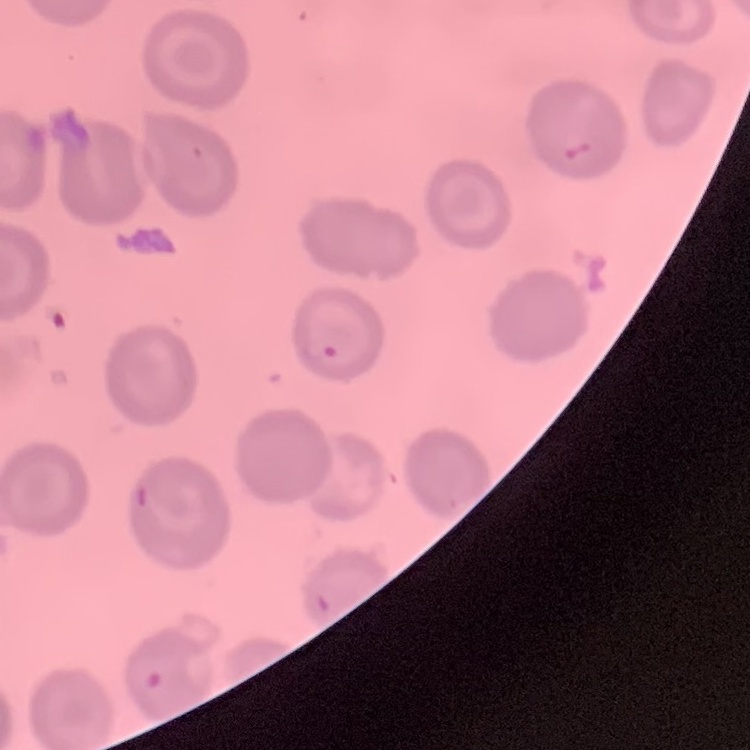
The erythrocytes show no rouleaux formation. Field's or Giemsa stain. Thin peripheral smear. One tile cut from a larger photomicrograph.